Outline each blood parasite and name the species.
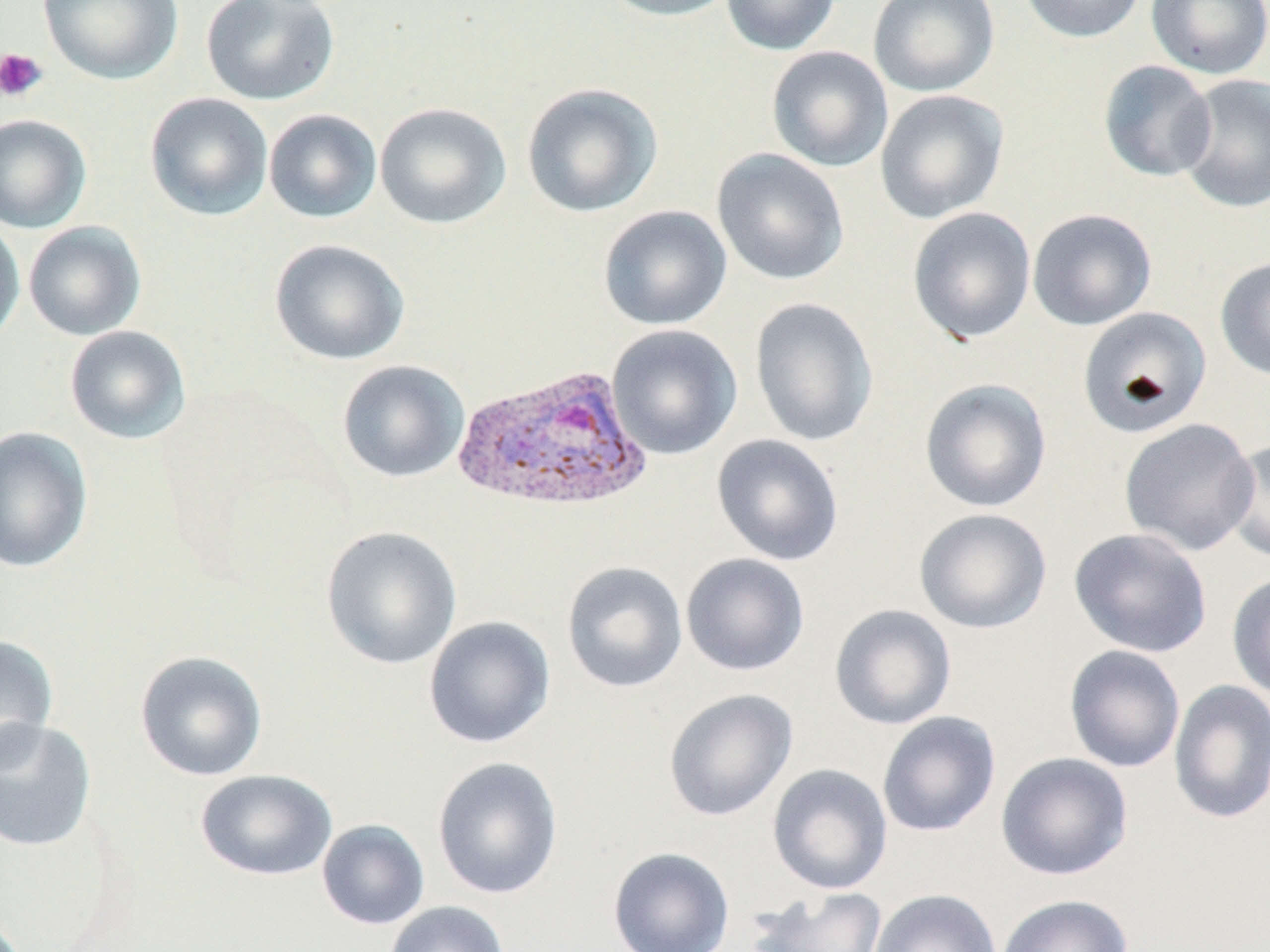
Approximate bounding boxes as named x1/y1/x2/y2 corners in pixels.
Plasmodium vivax-infected red blood cells: (x1=451, y1=364, x2=652, y2=515).
No Plasmodium falciparum, Plasmodium ovale, Plasmodium malariae, Babesia divergens, or Trypanosoma brucei observed.

Summary:
  - Uninfected red blood cell locations: (x1=38, y1=0, x2=183, y2=85), (x1=201, y1=0, x2=340, y2=106), (x1=598, y1=0, x2=741, y2=21), (x1=721, y1=0, x2=841, y2=55), (x1=868, y1=0, x2=1000, y2=97), (x1=1019, y1=0, x2=1147, y2=44), (x1=1146, y1=0, x2=1270, y2=80), (x1=766, y1=46, x2=893, y2=172), (x1=1098, y1=60, x2=1217, y2=182), (x1=1176, y1=74, x2=1270, y2=214), (x1=521, y1=82, x2=663, y2=218), (x1=874, y1=89, x2=1009, y2=224), (x1=144, y1=93, x2=273, y2=221), (x1=375, y1=102, x2=512, y2=229), (x1=263, y1=109, x2=382, y2=223), (x1=0, y1=114, x2=92, y2=233), (x1=711, y1=148, x2=850, y2=286), (x1=598, y1=205, x2=732, y2=330), (x1=907, y1=207, x2=1036, y2=344), (x1=1027, y1=208, x2=1157, y2=331), (x1=0, y1=217, x2=25, y2=347), (x1=23, y1=221, x2=146, y2=341), (x1=269, y1=239, x2=410, y2=366), (x1=1215, y1=257, x2=1270, y2=382), (x1=749, y1=296, x2=880, y2=448), (x1=1077, y1=306, x2=1212, y2=438), (x1=606, y1=324, x2=743, y2=459), (x1=64, y1=325, x2=192, y2=444), (x1=337, y1=360, x2=470, y2=483), (x1=919, y1=378, x2=1052, y2=513), (x1=1119, y1=418, x2=1260, y2=556), (x1=0, y1=426, x2=93, y2=573), (x1=711, y1=434, x2=845, y2=566), (x1=1224, y1=437, x2=1269, y2=565), (x1=914, y1=508, x2=1052, y2=634), (x1=320, y1=525, x2=462, y2=671), (x1=1069, y1=527, x2=1212, y2=658), (x1=680, y1=552, x2=810, y2=677), (x1=561, y1=560, x2=688, y2=693), (x1=1226, y1=572, x2=1270, y2=701), (x1=829, y1=604, x2=957, y2=730), (x1=423, y1=615, x2=556, y2=749), (x1=0, y1=633, x2=58, y2=770), (x1=1064, y1=645, x2=1186, y2=773), (x1=134, y1=650, x2=268, y2=782), (x1=1168, y1=680, x2=1270, y2=824), (x1=663, y1=688, x2=798, y2=821), (x1=877, y1=711, x2=1001, y2=837), (x1=0, y1=717, x2=97, y2=853), (x1=995, y1=752, x2=1133, y2=881), (x1=431, y1=756, x2=563, y2=900), (x1=767, y1=763, x2=893, y2=895), (x1=195, y1=768, x2=338, y2=881), (x1=316, y1=819, x2=430, y2=930), (x1=607, y1=847, x2=734, y2=952), (x1=748, y1=886, x2=889, y2=952), (x1=868, y1=888, x2=1002, y2=952), (x1=995, y1=893, x2=1133, y2=952), (x1=385, y1=900, x2=510, y2=952)
  - Platelet locations: (x1=0, y1=47, x2=48, y2=102)
  - Slide-level diagnosis: Plasmodium vivax
  - Magnification: 1000x
  - Preparation: thin blood film
  - Field of view: one of a larger specimen
  - Image size: 1270×952 pixels
  - Modality: light microscopy
  - Stain: May-Grünwald-Giemsa